Classify this cell by malaria status.
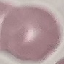

Uninfected.

{
  "stain": "Giemsa",
  "image_type": "cell patch, automatically extracted from a larger field of view and resized to 64 × 64 pixels",
  "capture": "smartphone through the microscope eyepiece",
  "preparation": "thin smear"
}